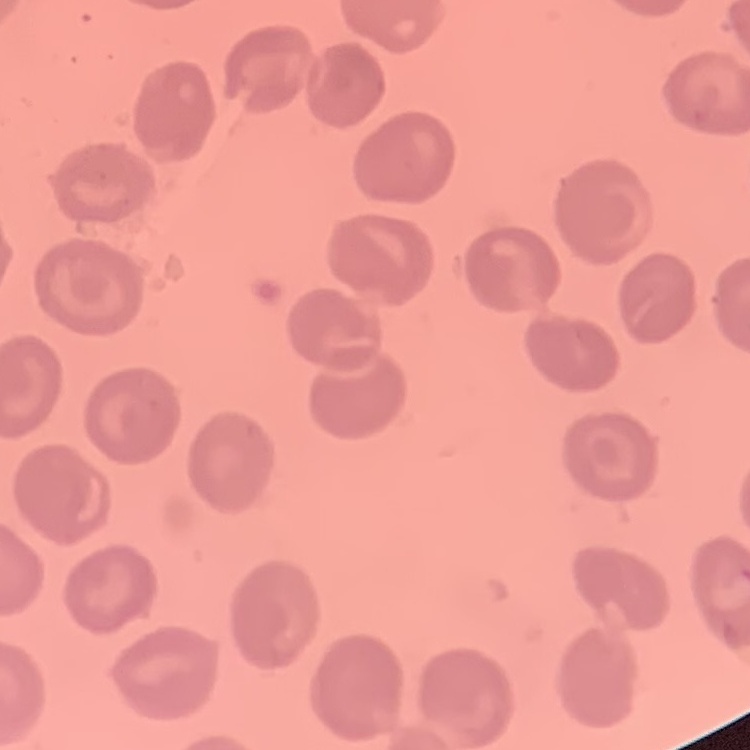
red_blood_cell_morphology: no rouleaux formation
stain: Field's or Giemsa
image_type: one tile cut from a larger photomicrograph
preparation: thin blood film